Outline each blood parasite and name the species.
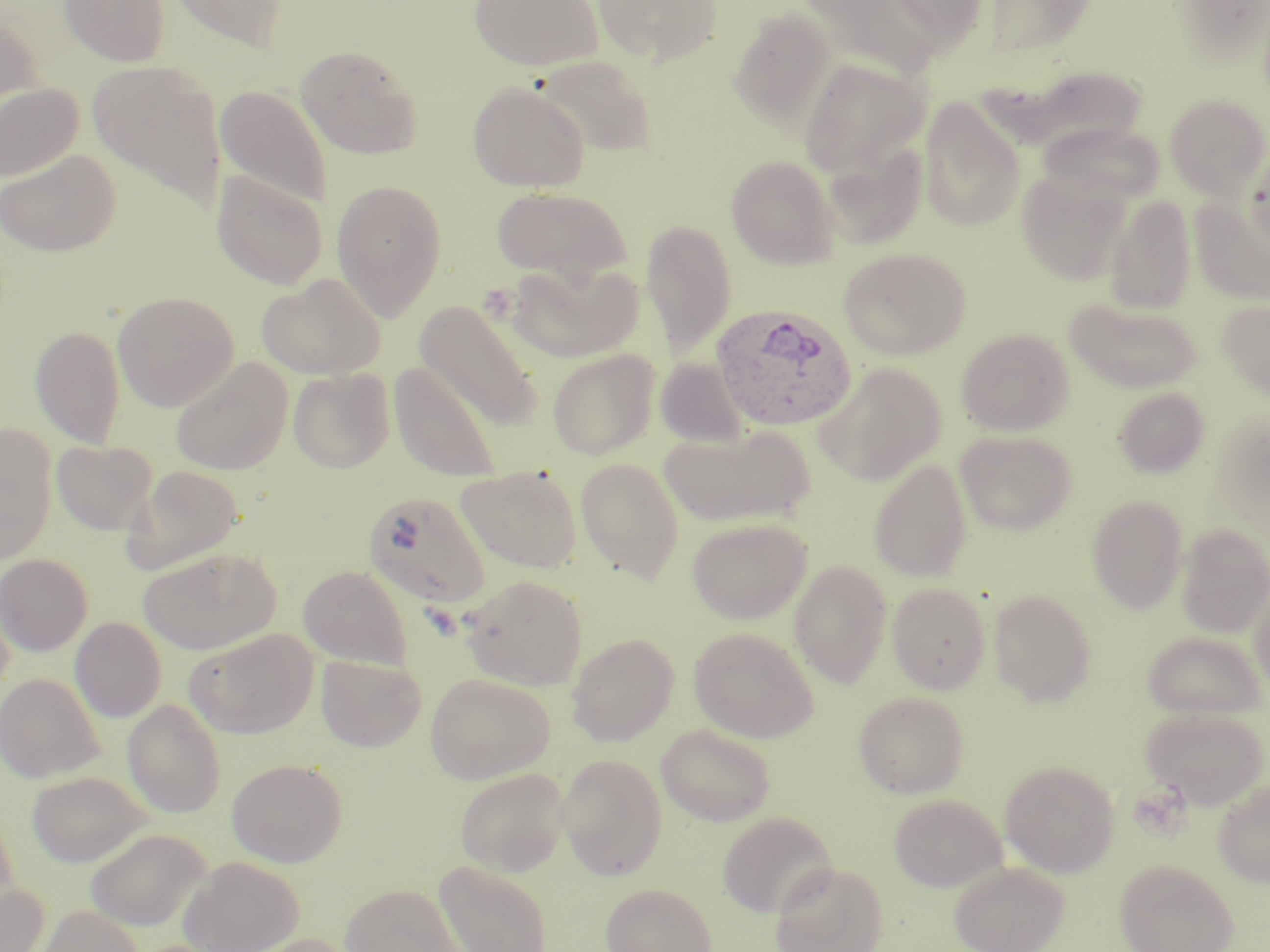

Approximate bounding boxes as [x1, y1, x2, y2] in pixels.
Plasmodium ovale-infected red blood cells: [711, 304, 858, 431].
No Plasmodium falciparum, Plasmodium malariae, Plasmodium vivax, Babesia divergens, or Trypanosoma brucei observed.

Uninfected red blood cell locations: [59, 0, 171, 66], [166, 0, 287, 51], [468, 0, 604, 71], [592, 0, 723, 65], [801, 0, 942, 83], [876, 0, 992, 56], [1169, 0, 1270, 67], [980, 1, 1099, 59], [728, 8, 837, 130], [0, 12, 40, 124], [296, 44, 423, 159], [535, 54, 658, 157], [797, 57, 927, 177], [87, 59, 228, 209], [467, 80, 589, 192], [0, 82, 83, 182], [215, 85, 332, 210], [1164, 93, 1269, 200], [919, 95, 1027, 232], [1039, 122, 1163, 205], [822, 140, 929, 250], [1242, 148, 1270, 258], [0, 149, 120, 256], [725, 154, 839, 269], [1017, 167, 1132, 285], [211, 170, 329, 290], [331, 180, 447, 321], [490, 186, 634, 285], [1104, 195, 1196, 314], [1190, 197, 1270, 304], [640, 218, 736, 357], [837, 247, 971, 360], [506, 260, 643, 362], [257, 273, 386, 380], [112, 291, 239, 411], [1064, 297, 1202, 393], [1216, 298, 1270, 402], [415, 299, 543, 431], [31, 324, 125, 449], [956, 328, 1074, 435], [547, 348, 660, 459], [171, 357, 293, 475], [655, 358, 749, 447], [388, 362, 504, 483], [814, 363, 947, 486], [288, 367, 394, 473], [1112, 387, 1211, 478], [0, 424, 57, 567], [658, 424, 815, 528], [955, 430, 1077, 535], [52, 439, 157, 534], [575, 457, 685, 583], [868, 458, 972, 581], [121, 465, 245, 575], [456, 465, 583, 573], [364, 491, 493, 609], [1085, 495, 1188, 613], [688, 516, 812, 624], [1176, 524, 1270, 638], [138, 548, 282, 655], [0, 553, 93, 655], [789, 560, 892, 688], [298, 565, 412, 669], [460, 573, 588, 689], [887, 582, 991, 694], [1250, 583, 1270, 702], [988, 589, 1097, 707], [70, 617, 166, 721], [688, 627, 819, 743], [185, 629, 319, 738], [1142, 631, 1267, 721], [566, 633, 679, 745], [316, 654, 427, 752], [0, 673, 105, 783], [425, 673, 556, 783], [853, 691, 969, 798], [123, 698, 226, 817], [1140, 706, 1269, 809], [656, 723, 776, 826], [557, 753, 667, 880], [227, 758, 347, 866], [1000, 760, 1120, 876], [454, 767, 570, 877], [27, 770, 154, 867], [1212, 778, 1270, 887], [888, 793, 1006, 891], [0, 806, 19, 919], [717, 811, 835, 916], [84, 828, 212, 930], [179, 855, 305, 951], [1115, 859, 1237, 952], [434, 860, 553, 952], [770, 861, 888, 952], [949, 861, 1069, 952], [339, 883, 464, 952], [601, 883, 717, 952], [0, 884, 50, 951], [35, 904, 143, 952], [240, 933, 361, 952]. Slide-level diagnosis: Plasmodium ovale. Optical microscopy. One field of a larger specimen. 1000x magnification. Image is 1270×952 pixels. Thin blood film. May-Grünwald-Giemsa stain.